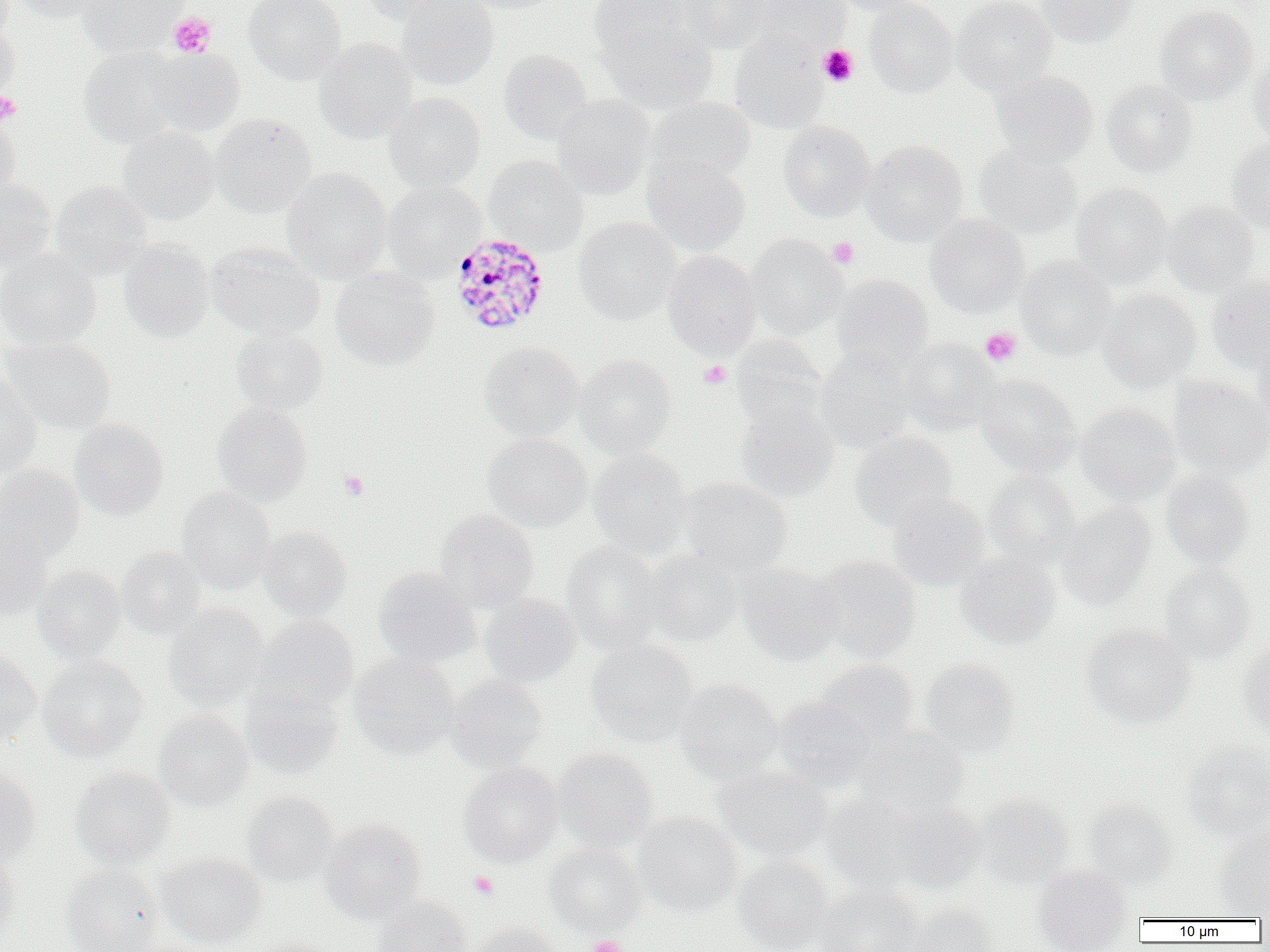

slide_level_diagnosis: Plasmodium malariae
magnification: 1000x
plasmodium_malariae_infected_red_blood_cell_locations: 'approximate bounding boxes as named x1/y1/x2/y2 corners in pixels: (x1=450, y1=232, x2=550, y2=336)'
preparation: thin blood film
modality: optical microscopy
field_of_view: single
uninfected_red_blood_cell_locations: 'approximate bounding boxes as named x1/y1/x2/y2 corners in pixels: (x1=0, y1=0, x2=19, y2=38), (x1=8, y1=0, x2=110, y2=24), (x1=77, y1=0, x2=188, y2=57), (x1=244, y1=0, x2=346, y2=84), (x1=361, y1=0, x2=466, y2=28), (x1=397, y1=0, x2=498, y2=90), (x1=457, y1=0, x2=562, y2=14), (x1=589, y1=0, x2=692, y2=59), (x1=678, y1=0, x2=774, y2=53), (x1=749, y1=0, x2=851, y2=54), (x1=831, y1=0, x2=925, y2=16), (x1=864, y1=0, x2=958, y2=97), (x1=952, y1=0, x2=1057, y2=95), (x1=1036, y1=0, x2=1139, y2=47), (x1=1155, y1=4, x2=1258, y2=105), (x1=0, y1=17, x2=19, y2=105), (x1=600, y1=17, x2=717, y2=114), (x1=730, y1=34, x2=828, y2=132), (x1=314, y1=38, x2=417, y2=143), (x1=78, y1=46, x2=186, y2=148), (x1=147, y1=48, x2=245, y2=136), (x1=499, y1=49, x2=594, y2=145), (x1=1247, y1=56, x2=1270, y2=149), (x1=990, y1=69, x2=1098, y2=167), (x1=1101, y1=79, x2=1197, y2=177), (x1=384, y1=92, x2=485, y2=192), (x1=552, y1=94, x2=655, y2=199), (x1=648, y1=97, x2=755, y2=185), (x1=0, y1=112, x2=21, y2=203), (x1=208, y1=112, x2=316, y2=217), (x1=779, y1=121, x2=876, y2=221), (x1=118, y1=126, x2=219, y2=225), (x1=1227, y1=138, x2=1270, y2=233), (x1=862, y1=139, x2=968, y2=246), (x1=974, y1=144, x2=1082, y2=241), (x1=642, y1=153, x2=751, y2=256), (x1=483, y1=156, x2=589, y2=255), (x1=282, y1=169, x2=391, y2=284), (x1=0, y1=177, x2=55, y2=275), (x1=50, y1=181, x2=152, y2=279), (x1=382, y1=182, x2=485, y2=281), (x1=1071, y1=184, x2=1173, y2=286), (x1=1161, y1=201, x2=1260, y2=297), (x1=925, y1=215, x2=1029, y2=318), (x1=574, y1=218, x2=681, y2=323), (x1=746, y1=235, x2=848, y2=340), (x1=119, y1=240, x2=214, y2=342), (x1=207, y1=243, x2=324, y2=340), (x1=0, y1=249, x2=100, y2=350), (x1=662, y1=250, x2=761, y2=358), (x1=1017, y1=256, x2=1117, y2=360), (x1=331, y1=267, x2=439, y2=370), (x1=832, y1=275, x2=934, y2=374), (x1=1206, y1=276, x2=1270, y2=374), (x1=1099, y1=289, x2=1201, y2=392), (x1=231, y1=326, x2=328, y2=415), (x1=1252, y1=335, x2=1270, y2=427), (x1=730, y1=336, x2=826, y2=430), (x1=2, y1=337, x2=115, y2=434), (x1=900, y1=339, x2=999, y2=435), (x1=479, y1=341, x2=583, y2=440), (x1=815, y1=350, x2=917, y2=452), (x1=575, y1=354, x2=677, y2=456), (x1=0, y1=375, x2=42, y2=478), (x1=976, y1=375, x2=1081, y2=477), (x1=1167, y1=375, x2=1270, y2=479), (x1=733, y1=402, x2=838, y2=501), (x1=212, y1=403, x2=313, y2=505), (x1=1076, y1=403, x2=1180, y2=505), (x1=69, y1=419, x2=169, y2=520), (x1=850, y1=431, x2=958, y2=532), (x1=483, y1=433, x2=592, y2=533), (x1=588, y1=449, x2=692, y2=558), (x1=0, y1=465, x2=84, y2=562), (x1=985, y1=470, x2=1081, y2=567), (x1=1161, y1=471, x2=1255, y2=568), (x1=679, y1=478, x2=792, y2=575), (x1=177, y1=489, x2=277, y2=593), (x1=887, y1=494, x2=991, y2=591), (x1=1057, y1=502, x2=1155, y2=610), (x1=434, y1=508, x2=539, y2=611), (x1=0, y1=520, x2=53, y2=622), (x1=259, y1=527, x2=352, y2=620), (x1=562, y1=541, x2=663, y2=654), (x1=116, y1=546, x2=206, y2=638), (x1=641, y1=549, x2=743, y2=646), (x1=955, y1=552, x2=1061, y2=648), (x1=813, y1=556, x2=921, y2=663), (x1=737, y1=563, x2=845, y2=665), (x1=32, y1=565, x2=126, y2=664), (x1=1159, y1=565, x2=1255, y2=663), (x1=373, y1=567, x2=479, y2=667), (x1=479, y1=593, x2=581, y2=687), (x1=163, y1=604, x2=269, y2=710), (x1=253, y1=615, x2=359, y2=714), (x1=1082, y1=625, x2=1195, y2=727), (x1=586, y1=639, x2=697, y2=747), (x1=1238, y1=641, x2=1270, y2=740), (x1=0, y1=648, x2=42, y2=746), (x1=349, y1=653, x2=460, y2=759), (x1=38, y1=656, x2=147, y2=762), (x1=920, y1=658, x2=1019, y2=754), (x1=816, y1=659, x2=920, y2=746), (x1=446, y1=676, x2=547, y2=772), (x1=675, y1=679, x2=782, y2=783), (x1=240, y1=681, x2=344, y2=780), (x1=773, y1=696, x2=876, y2=790), (x1=154, y1=710, x2=254, y2=811), (x1=854, y1=727, x2=969, y2=817), (x1=1182, y1=743, x2=1270, y2=841), (x1=554, y1=748, x2=658, y2=850), (x1=458, y1=761, x2=563, y2=866), (x1=713, y1=766, x2=832, y2=861), (x1=70, y1=767, x2=175, y2=870), (x1=0, y1=768, x2=41, y2=867), (x1=243, y1=791, x2=338, y2=887), (x1=977, y1=794, x2=1074, y2=888), (x1=823, y1=795, x2=925, y2=892), (x1=1084, y1=799, x2=1177, y2=888), (x1=892, y1=803, x2=989, y2=892), (x1=634, y1=812, x2=742, y2=915), (x1=320, y1=818, x2=426, y2=923), (x1=1215, y1=826, x2=1270, y2=917), (x1=544, y1=843, x2=645, y2=937), (x1=0, y1=849, x2=21, y2=943), (x1=157, y1=852, x2=266, y2=948), (x1=734, y1=856, x2=833, y2=952), (x1=60, y1=864, x2=165, y2=952), (x1=1033, y1=865, x2=1133, y2=952), (x1=818, y1=885, x2=922, y2=952), (x1=374, y1=896, x2=471, y2=952), (x1=908, y1=903, x2=1000, y2=952), (x1=467, y1=922, x2=562, y2=952), (x1=245, y1=937, x2=334, y2=952)'
image_size: 1270×952 pixels
platelet_locations: 'approximate bounding boxes as named x1/y1/x2/y2 corners in pixels: (x1=168, y1=13, x2=216, y2=58), (x1=818, y1=45, x2=858, y2=87), (x1=0, y1=90, x2=21, y2=126), (x1=827, y1=237, x2=859, y2=269), (x1=980, y1=327, x2=1021, y2=366), (x1=698, y1=360, x2=732, y2=388), (x1=339, y1=472, x2=369, y2=500), (x1=468, y1=871, x2=498, y2=899), (x1=588, y1=935, x2=626, y2=952)'